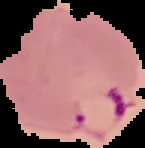
Summary:
  - Image type: segmented cell region on a black background
  - Image size: 145×148 pixels
  - Malaria status: parasitized
  - Preparation: thin blood smear